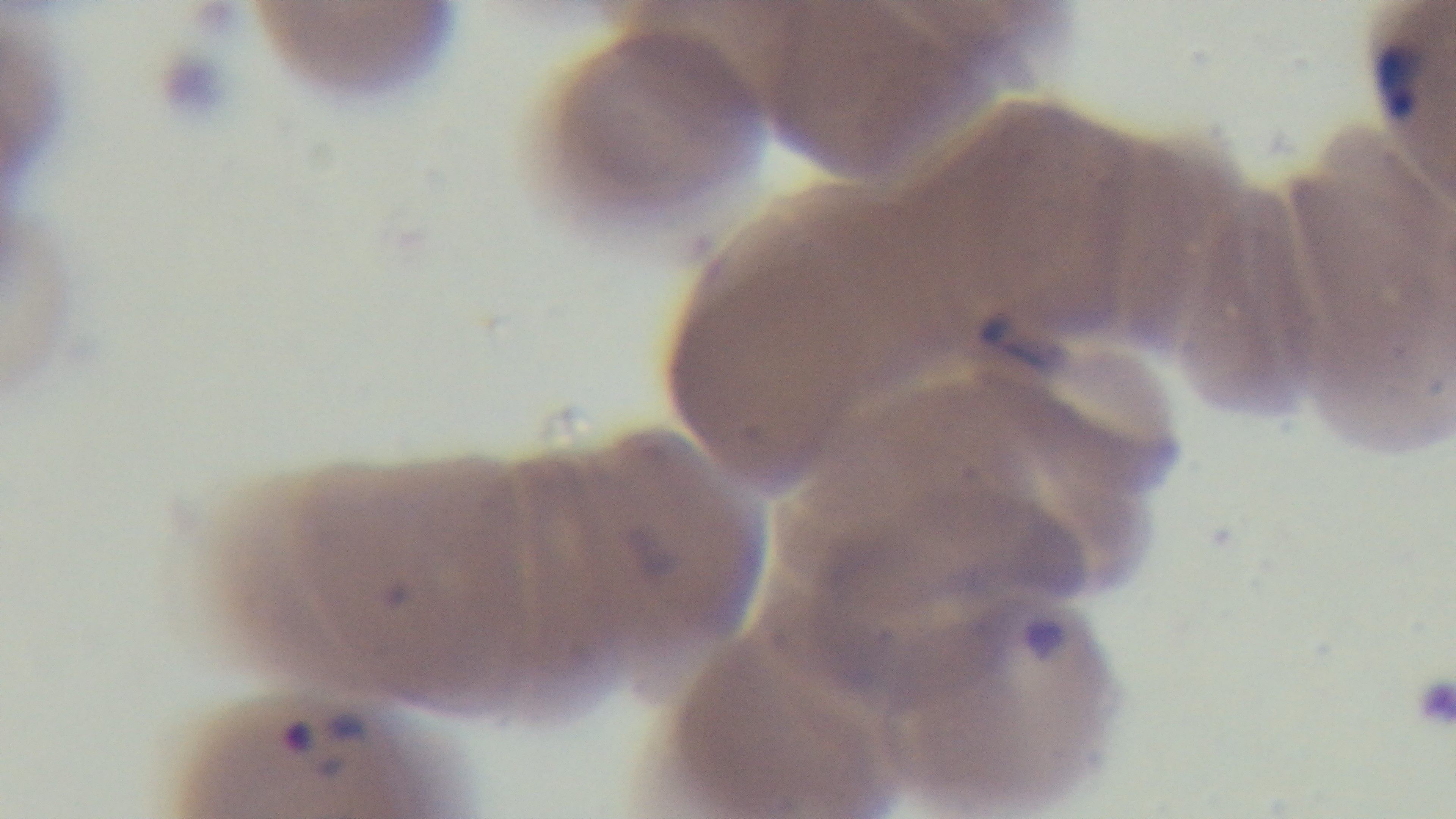

Summary:
  - Malaria status: infected
  - Capture: mounted 4K digital camera
  - Field of view: single
  - Modality: light microscopy
  - Stain: Giemsa
  - Preparation: thin
  - Objective: 100x oil immersion